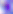

{
  "identification": "Toxoplasma gondii",
  "modality": "micrograph",
  "magnification": "400x"
}